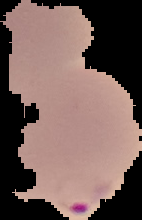

From a thin blood film. Malaria status: parasitized. Cell region segmented out of the field of view; the surrounding area is masked to black. Image is 142×220 pixels.